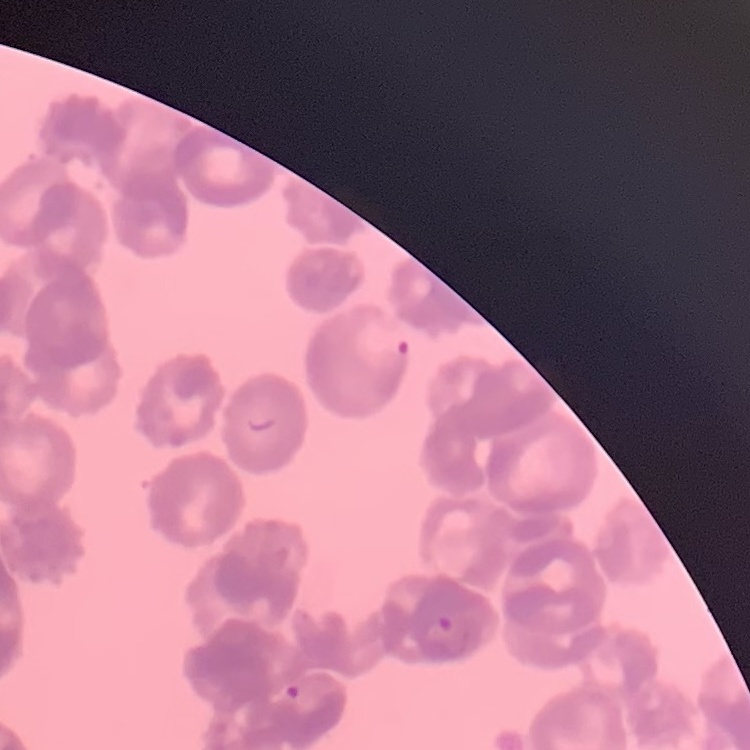

Summary:
  - Red blood cell morphology: rouleaux formation
  - Image type: one tile cut from a larger photomicrograph
  - Preparation: thin blood smear
  - Stain: Field's or Giemsa